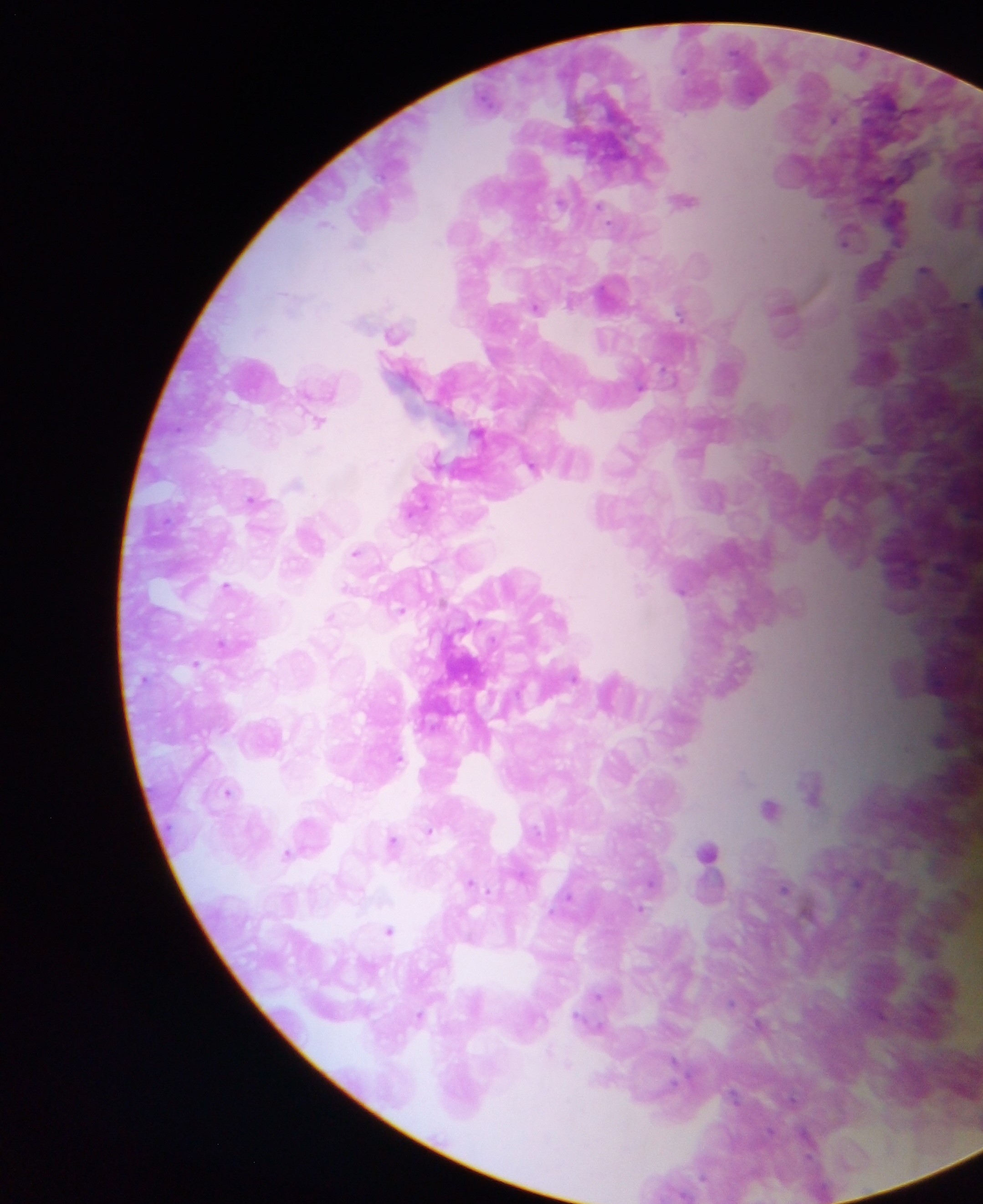
Approximate centers as (x, y) in pixels. Malaria parasite locations: (686, 199), (897, 210), (848, 236), (925, 271), (613, 289), (536, 306), (785, 308), (395, 332), (317, 420), (478, 431), (439, 462), (532, 466), (255, 499), (416, 500), (356, 552), (226, 586), (681, 589), (400, 610), (330, 617), (196, 664), (942, 738), (397, 757), (813, 787), (227, 792), (769, 807), (429, 831), (392, 842), (706, 851), (287, 853), (471, 883), (784, 888), (390, 929), (599, 995), (420, 1016). Collected in Ghana. Image is 983×1204 pixels. Mobile-phone photograph taken through the microscope. One field of view. Thick blood film.